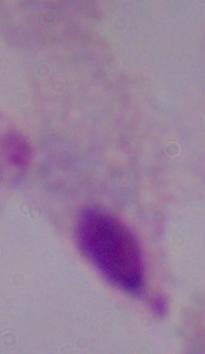
Captured at 1000x magnification. Micrograph. A trichomonad is shown.